Classify this cell by malaria status.
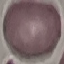
Uninfected.

stain = Giemsa
image type = automatically extracted cell patch, resized to 64 × 64 pixels
preparation = thin smear
capture = smartphone camera at the microscope eyepiece